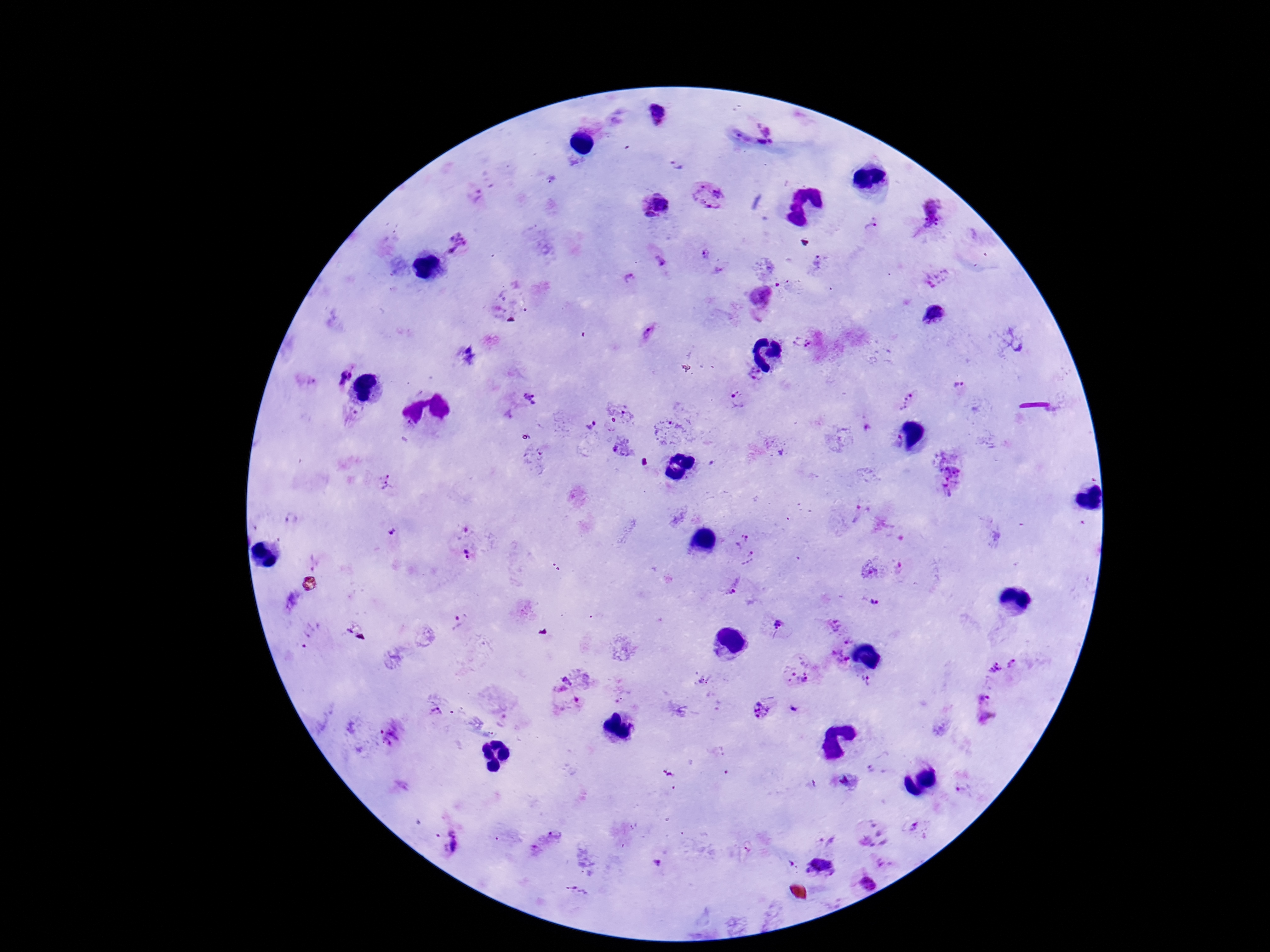
Plasmodium parasite locations = approximate centers as (x, y) in pixels: (655, 114), (768, 134), (677, 166), (708, 193), (477, 196), (655, 204), (931, 212), (872, 228), (462, 243), (704, 254), (660, 260), (818, 262), (630, 278), (939, 278), (762, 293), (935, 313), (649, 333), (802, 343), (343, 376), (755, 378), (959, 385), (531, 398), (737, 400), (907, 402), (591, 426), (622, 449), (777, 450), (951, 480), (387, 481), (392, 534), (744, 538), (468, 554), (752, 559), (875, 567), (738, 589), (874, 598), (459, 621), (779, 625), (844, 627), (841, 661), (1003, 665), (797, 669), (576, 677), (866, 679), (981, 697), (435, 710), (763, 710), (989, 719), (393, 734), (844, 781), (965, 788), (915, 830), (873, 834), (451, 841), (547, 841), (826, 841), (659, 862), (885, 864), (867, 884), (578, 891)
preparation = thick blood film
magnification = 100x
patient malaria status = infected
field of view = single
stain = Giemsa
image size = 1270×952 pixels
capture = smartphone camera through the microscope eyepiece